Classify this cell by malaria status.
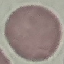
It is uninfected.

Summary:
  - Image type: automatically extracted cell patch, resized to 64 × 64 pixels
  - Stain: Giemsa
  - Preparation: thin blood film
  - Capture: smartphone camera at the microscope eyepiece